Identify the parasite.
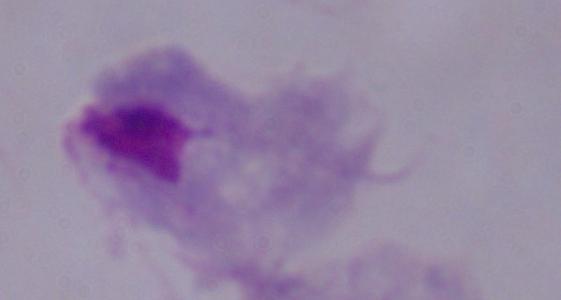

This is a trichomonad.

Summary:
  - Magnification: 1000x
  - Modality: micrograph